Rate the background quality.
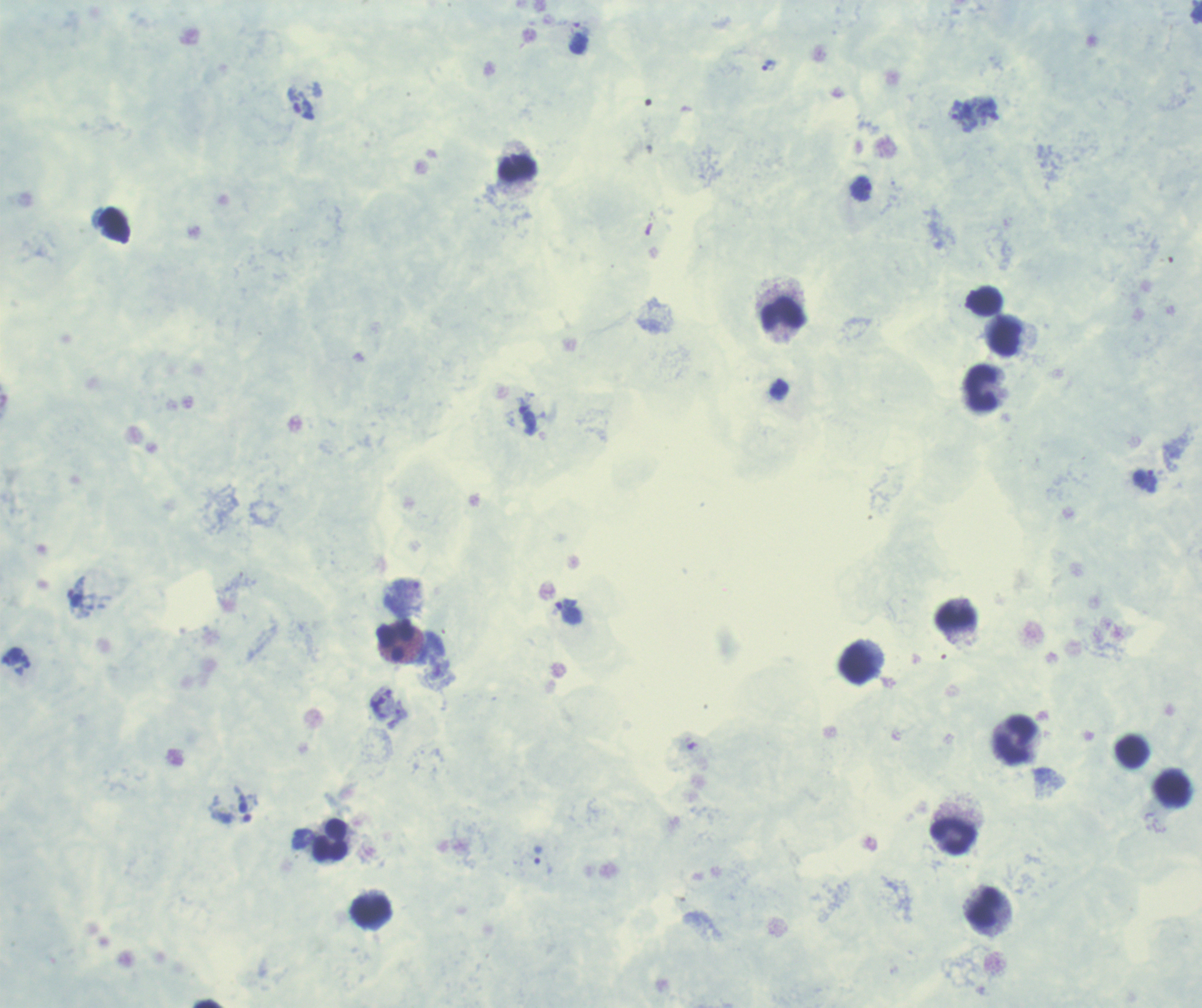

Unsatisfactory.

Approximate centers as (x, y) in pixels. Leukocyte locations: (518, 168), (784, 314), (1005, 338), (981, 388), (956, 617), (396, 641), (857, 663), (1015, 739), (1132, 751), (1171, 790), (953, 837), (330, 840), (983, 906), (370, 911). Trophozoite locations: (769, 65), (301, 103), (963, 116), (861, 189), (1145, 482), (567, 611), (11, 656), (304, 839), (538, 855). One field from this slide. Result: malaria parasites identified. Previously used in an actual diagnosis. Romanowsky stain. Image is 1202×1008 pixels. Thick smear of blood. 100x magnification.